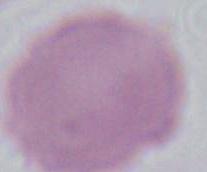

Summary:
  - Modality: micrograph
  - Magnification: 1000x
  - Identification: red blood cell